Assess for malaria.
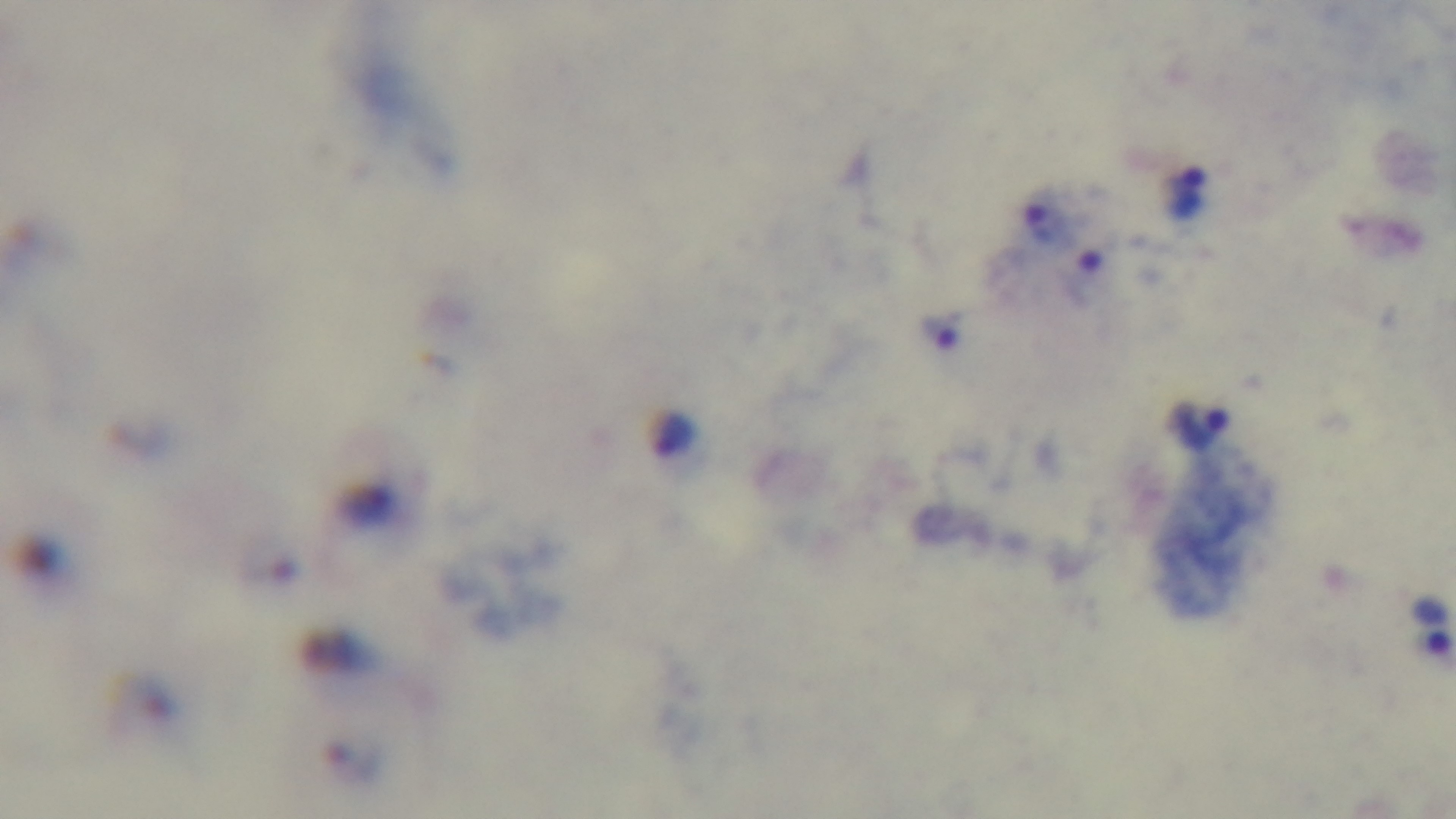
Positive.

Preparation: thick. Single field of view. Mounted 4K digital camera. Photomicrograph. 100x oil-immersion objective. Giemsa-stained.